Give the extent of all uninfected red blood cells.
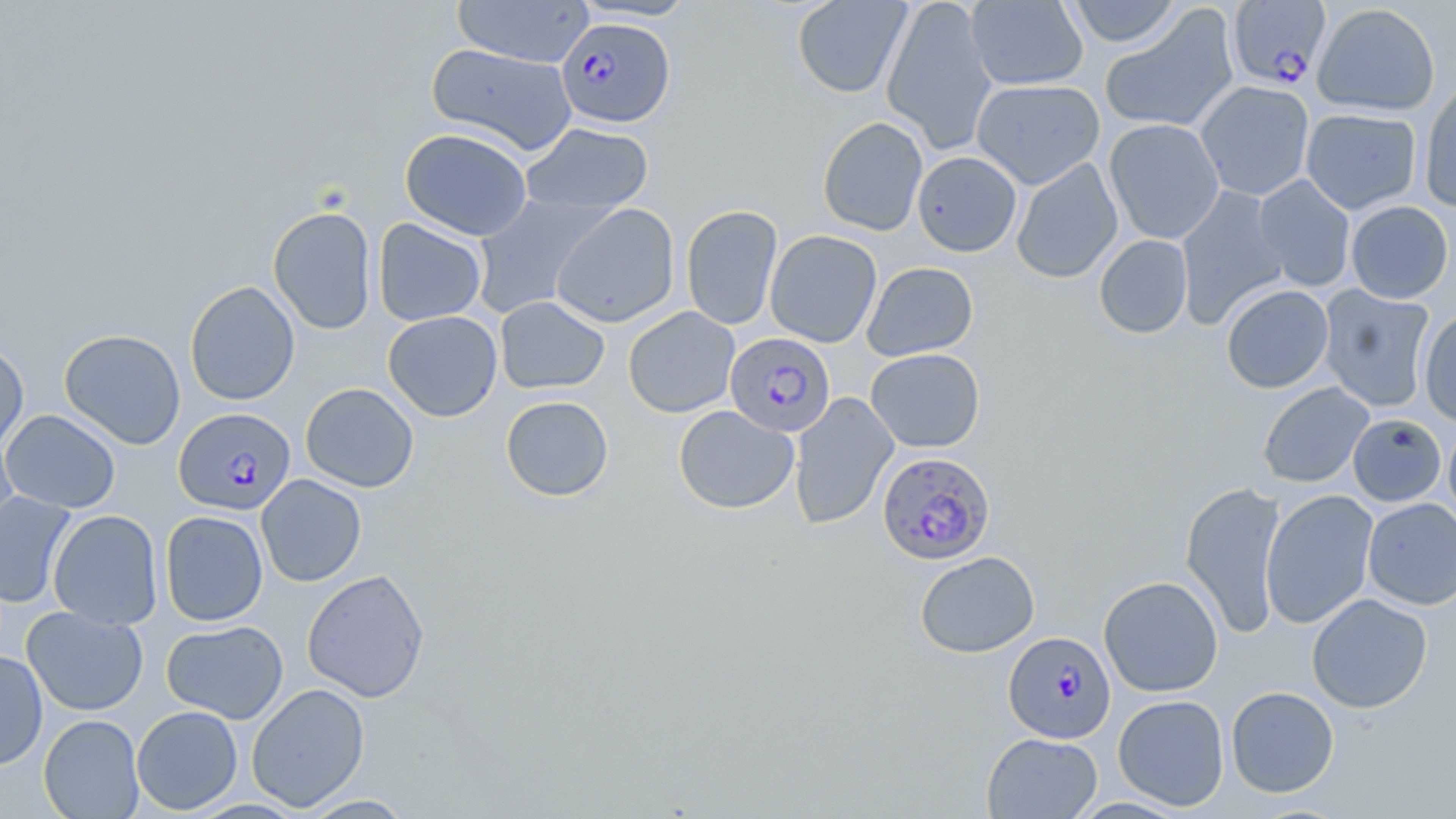
Approximate bounding boxes as named x1/y1/x2/y2 corners in pixels.
Uninfected red blood cells: (x1=452, y1=0, x2=594, y2=68), (x1=570, y1=0, x2=700, y2=22), (x1=792, y1=0, x2=911, y2=98), (x1=881, y1=0, x2=999, y2=154), (x1=966, y1=0, x2=1088, y2=91), (x1=1063, y1=0, x2=1184, y2=48), (x1=1312, y1=3, x2=1441, y2=116), (x1=1099, y1=4, x2=1239, y2=135), (x1=427, y1=43, x2=577, y2=157), (x1=971, y1=78, x2=1105, y2=189), (x1=1195, y1=80, x2=1314, y2=201), (x1=1419, y1=80, x2=1456, y2=212), (x1=1301, y1=107, x2=1422, y2=214), (x1=817, y1=116, x2=928, y2=236), (x1=1103, y1=118, x2=1225, y2=244), (x1=520, y1=122, x2=654, y2=217), (x1=399, y1=128, x2=533, y2=240), (x1=912, y1=151, x2=1022, y2=256), (x1=1011, y1=158, x2=1123, y2=284), (x1=1252, y1=174, x2=1356, y2=292), (x1=1175, y1=185, x2=1291, y2=329), (x1=470, y1=193, x2=611, y2=319), (x1=1345, y1=200, x2=1454, y2=304), (x1=551, y1=203, x2=680, y2=328), (x1=681, y1=204, x2=783, y2=330), (x1=267, y1=206, x2=377, y2=335), (x1=373, y1=218, x2=487, y2=326), (x1=765, y1=230, x2=882, y2=347), (x1=1094, y1=234, x2=1193, y2=339), (x1=862, y1=261, x2=978, y2=361), (x1=185, y1=281, x2=300, y2=406), (x1=1221, y1=284, x2=1334, y2=394), (x1=1317, y1=284, x2=1436, y2=412), (x1=495, y1=296, x2=610, y2=394), (x1=623, y1=306, x2=740, y2=418), (x1=1418, y1=309, x2=1456, y2=427), (x1=383, y1=311, x2=503, y2=422), (x1=59, y1=329, x2=186, y2=450), (x1=0, y1=340, x2=29, y2=454), (x1=865, y1=348, x2=985, y2=452), (x1=1257, y1=382, x2=1374, y2=488), (x1=300, y1=383, x2=419, y2=492), (x1=788, y1=392, x2=899, y2=530), (x1=500, y1=395, x2=614, y2=502), (x1=673, y1=405, x2=798, y2=514), (x1=1, y1=409, x2=121, y2=514), (x1=1347, y1=414, x2=1447, y2=506), (x1=1443, y1=419, x2=1456, y2=529), (x1=1, y1=431, x2=20, y2=548), (x1=256, y1=474, x2=366, y2=587), (x1=1180, y1=480, x2=1287, y2=640), (x1=1260, y1=489, x2=1378, y2=629), (x1=0, y1=491, x2=77, y2=608), (x1=1362, y1=498, x2=1456, y2=609), (x1=48, y1=509, x2=164, y2=630), (x1=160, y1=511, x2=269, y2=626), (x1=915, y1=551, x2=1040, y2=658), (x1=302, y1=568, x2=430, y2=702), (x1=1098, y1=575, x2=1224, y2=697), (x1=1306, y1=593, x2=1433, y2=713), (x1=21, y1=606, x2=149, y2=716), (x1=161, y1=619, x2=288, y2=724), (x1=0, y1=650, x2=48, y2=770), (x1=246, y1=683, x2=369, y2=812), (x1=1225, y1=686, x2=1339, y2=797), (x1=1113, y1=694, x2=1230, y2=811), (x1=131, y1=705, x2=243, y2=814), (x1=38, y1=714, x2=145, y2=818), (x1=982, y1=732, x2=1102, y2=818), (x1=299, y1=794, x2=416, y2=818).

slide-level diagnosis = Plasmodium falciparum
preparation = thin blood smear
modality = light microscopy
Plasmodium falciparum-infected red blood cell locations = approximate bounding boxes as named x1/y1/x2/y2 corners in pixels: (x1=1227, y1=1, x2=1331, y2=90), (x1=556, y1=17, x2=674, y2=128), (x1=725, y1=331, x2=836, y2=437), (x1=174, y1=407, x2=296, y2=516), (x1=877, y1=451, x2=995, y2=564), (x1=1004, y1=631, x2=1116, y2=744)
image size = 1456×819 pixels
magnification = 1000x
field of view = one of a larger specimen
stain = May-Grünwald-Giemsa